Locate every malaria parasite.
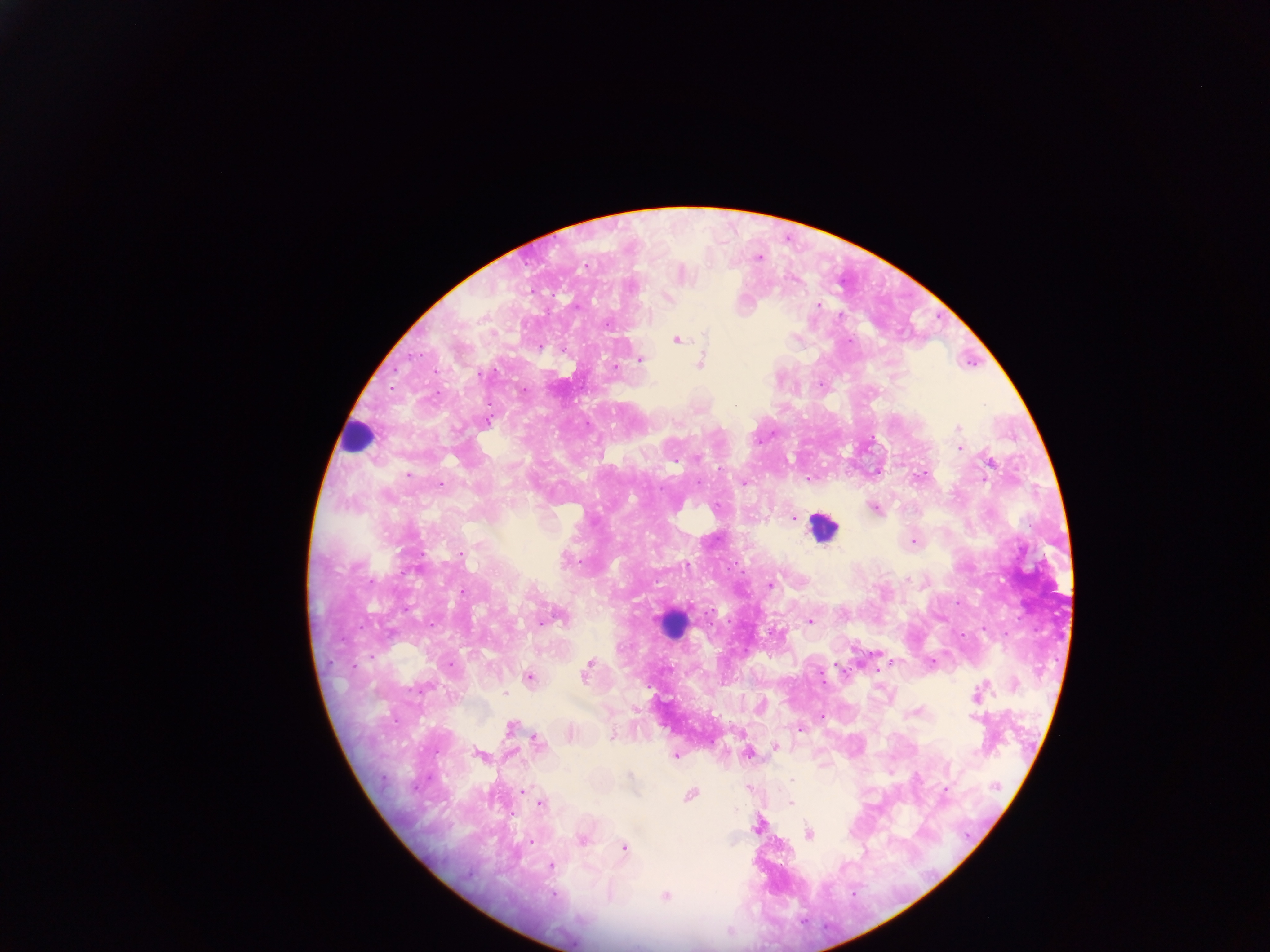
Approximate centers as (x, y) in pixels.
Malaria parasites: (758, 257), (681, 273), (667, 297), (817, 306), (677, 338), (847, 341), (639, 360), (701, 361), (616, 368), (486, 421), (957, 428), (959, 447), (988, 462), (877, 471), (408, 474), (918, 476), (743, 482), (440, 485), (873, 508), (793, 518), (913, 541), (460, 553), (769, 585), (552, 617), (809, 621), (874, 654), (893, 662), (931, 662), (836, 664), (448, 665), (877, 670), (586, 671), (529, 677), (977, 693), (761, 706), (916, 711), (821, 717), (510, 727), (800, 728), (570, 733), (612, 735), (537, 742), (775, 747), (747, 752), (480, 755), (675, 755), (890, 773), (749, 787), (523, 789), (945, 789), (689, 794), (540, 803), (789, 803), (758, 824), (808, 834), (581, 839), (623, 847), (550, 866), (665, 896).

Summary:
  - Leukocyte locations: (357, 437), (823, 528), (671, 624)
  - Preparation: thick blood smear
  - Field of view: single
  - Country: Ghana
  - Image size: 1270×952 pixels
  - Capture: mobile-phone photograph through a microscope